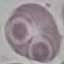

Summary:
  - Malaria status: uninfected
  - Image type: automatically extracted cell patch, resized to 64 × 64 pixels
  - Stain: Giemsa
  - Capture: smartphone camera at the microscope eyepiece
  - Preparation: thin blood film